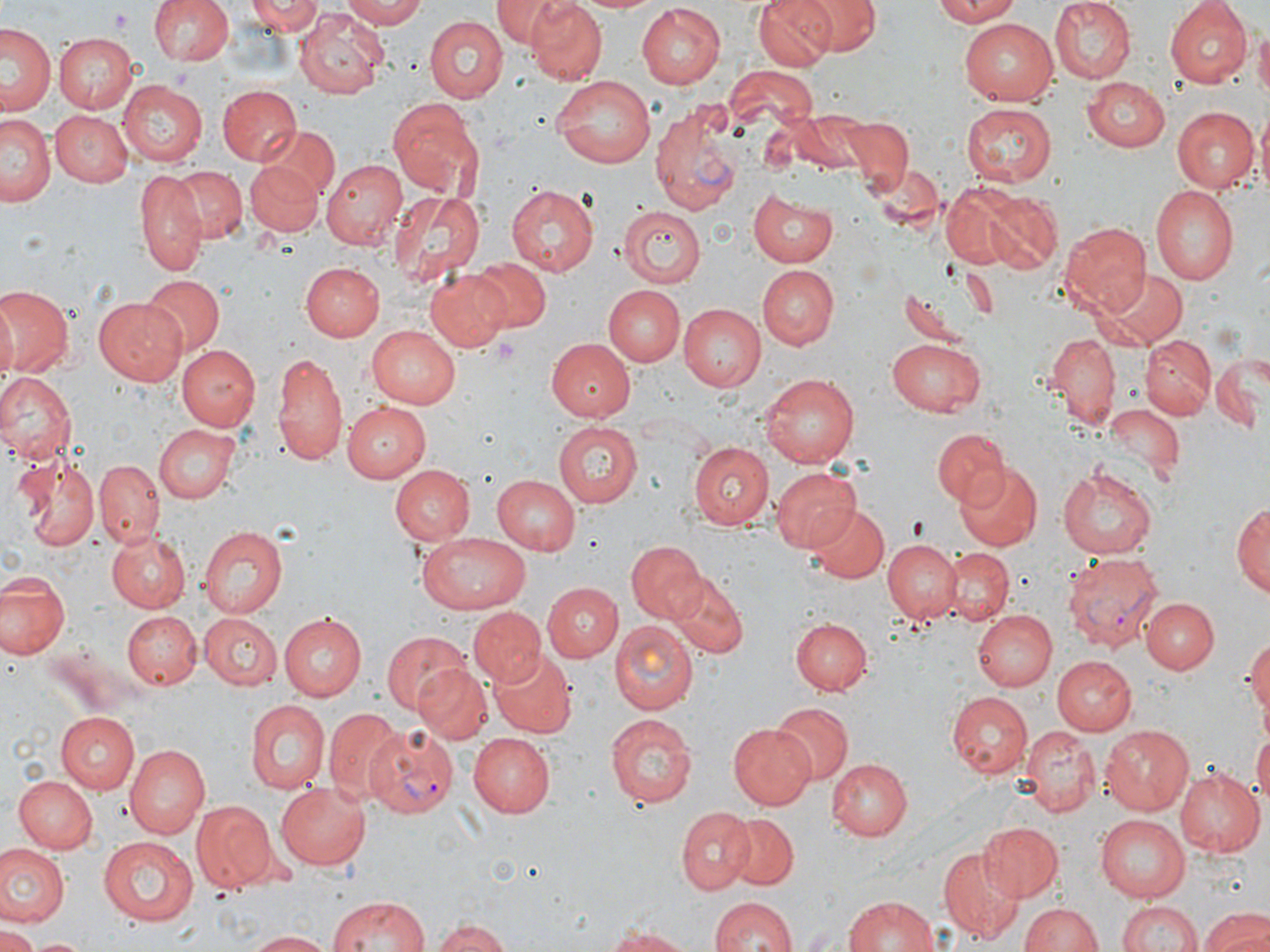

{
  "slide_level_diagnosis": "Plasmodium vivax",
  "modality": "light microscopy",
  "uninfected_red_blood_cell_locations": "approximate bounding boxes as [x1, y1, x2, y2] in pixels: [148, 0, 235, 67], [248, 0, 322, 35], [341, 0, 430, 27], [493, 0, 568, 45], [523, 0, 607, 84], [571, 0, 665, 14], [756, 0, 837, 70], [804, 0, 878, 53], [931, 0, 1026, 25], [1048, 0, 1134, 83], [1167, 0, 1255, 87], [635, 4, 726, 86], [297, 9, 387, 99], [960, 16, 1058, 101], [424, 17, 508, 102], [4, 22, 58, 118], [1253, 22, 1270, 104], [55, 31, 139, 113], [724, 67, 821, 137], [551, 73, 660, 170], [1084, 77, 1170, 151], [118, 81, 207, 164], [217, 85, 300, 167], [387, 96, 487, 202], [961, 102, 1056, 184], [1256, 106, 1270, 202], [1171, 107, 1257, 192], [792, 109, 872, 174], [49, 111, 132, 187], [3, 113, 58, 206], [841, 115, 912, 191], [262, 122, 337, 197], [866, 158, 943, 233], [323, 159, 405, 249], [243, 160, 321, 236], [170, 166, 247, 242], [136, 171, 208, 276], [505, 183, 599, 275], [939, 183, 1021, 266], [1152, 183, 1239, 286], [388, 188, 484, 287], [751, 188, 841, 265], [982, 192, 1064, 272], [619, 204, 705, 286], [1060, 221, 1150, 314], [473, 258, 550, 332], [298, 261, 384, 342], [758, 266, 838, 348], [425, 267, 514, 354], [1094, 267, 1189, 350], [141, 274, 223, 357], [0, 285, 74, 378], [602, 285, 684, 366], [95, 295, 190, 385], [678, 303, 766, 392], [366, 326, 461, 408], [1044, 334, 1121, 426], [1142, 334, 1216, 420], [887, 337, 988, 418], [546, 338, 637, 422], [175, 344, 260, 431], [270, 349, 348, 468], [1210, 352, 1266, 433], [761, 371, 863, 467], [0, 372, 74, 466], [341, 401, 430, 481], [1106, 403, 1185, 480], [554, 421, 642, 507], [155, 424, 239, 503], [931, 427, 1009, 509], [692, 440, 775, 529], [13, 455, 100, 553], [95, 460, 164, 545], [957, 464, 1042, 552], [390, 465, 475, 546], [770, 465, 862, 552], [1057, 466, 1160, 559], [492, 474, 582, 553], [1233, 499, 1268, 602], [807, 502, 889, 582], [198, 525, 288, 617], [107, 531, 189, 612], [417, 532, 532, 615], [884, 538, 963, 622], [627, 539, 705, 621], [943, 545, 1014, 625], [1, 571, 68, 660], [666, 572, 748, 658], [543, 583, 620, 661], [1141, 597, 1218, 673], [469, 606, 543, 684], [123, 610, 201, 688], [972, 610, 1057, 690], [279, 613, 366, 700], [199, 614, 283, 690], [791, 617, 873, 697], [611, 621, 698, 713], [381, 629, 470, 715], [1245, 635, 1270, 721], [488, 649, 575, 739], [1051, 656, 1137, 735], [412, 663, 491, 744], [946, 692, 1032, 780], [245, 699, 329, 794], [774, 704, 852, 783], [323, 707, 404, 802], [58, 710, 141, 792], [605, 714, 697, 807], [727, 722, 815, 809], [1101, 724, 1196, 815], [1019, 726, 1100, 816], [1251, 728, 1270, 813], [468, 732, 554, 815], [123, 742, 210, 838], [826, 759, 911, 839], [1174, 767, 1266, 857], [13, 774, 98, 852], [274, 783, 373, 870], [190, 800, 275, 892], [677, 805, 756, 894], [723, 813, 796, 889], [1096, 816, 1193, 903], [978, 821, 1064, 900], [99, 836, 200, 925], [0, 844, 68, 929], [939, 844, 1025, 941], [325, 894, 431, 952], [843, 894, 943, 952], [708, 896, 796, 952], [1119, 899, 1201, 952], [1018, 902, 1106, 952], [1199, 906, 1270, 952], [431, 916, 513, 952], [598, 925, 698, 950], [0, 927, 41, 952], [244, 930, 339, 951], [24, 937, 93, 952]",
  "field_of_view": "single",
  "preparation": "thin blood film",
  "stain": "May-Grünwald-Giemsa",
  "image_size": "1270×952 pixels",
  "plasmodium_vivax_infected_red_blood_cell_locations": "approximate bounding boxes as [x1, y1, x2, y2] in pixels: [649, 98, 747, 217], [1062, 550, 1165, 653], [365, 726, 459, 820]",
  "magnification": "1000x",
  "platelet_locations": "approximate bounding boxes as [x1, y1, x2, y2] in pixels: [109, 10, 134, 30], [492, 339, 521, 363], [906, 514, 930, 539]"
}